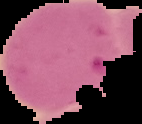
Segmented cell region on a black background. Image is 142×124 pixels. From a thin blood smear. Result: malaria parasites identified.